Comment on the morphology of the erythrocytes.
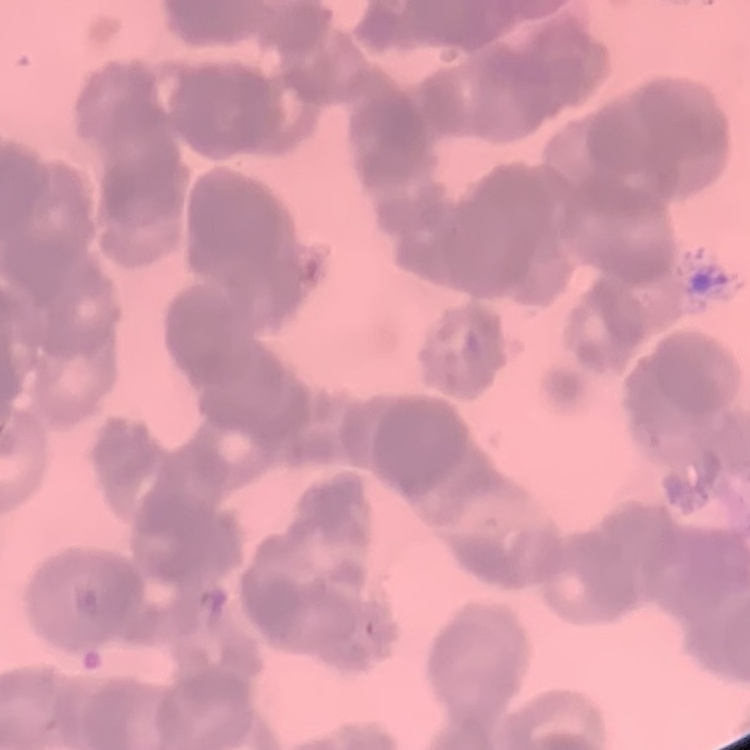

Rouleaux formation.

Summary:
  - Stain: Field's or Giemsa
  - Image type: one tile cut from a larger photomicrograph
  - Preparation: thin blood film